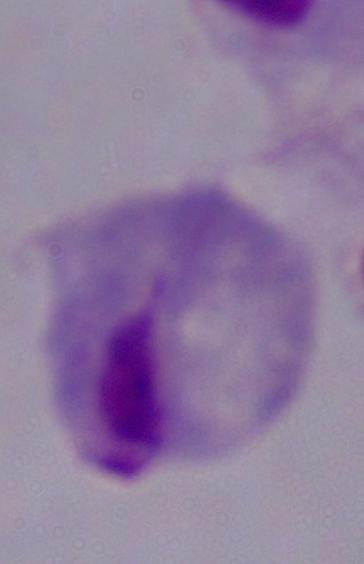
{
  "magnification": "1000x",
  "modality": "photomicrograph",
  "identification": "trichomonad"
}